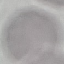

Summary:
  - Malaria status: uninfected
  - Preparation: thin blood smear
  - Stain: Giemsa
  - Image type: automatically extracted cell patch, resized to 64 × 64 pixels
  - Capture: smartphone camera at the microscope eyepiece